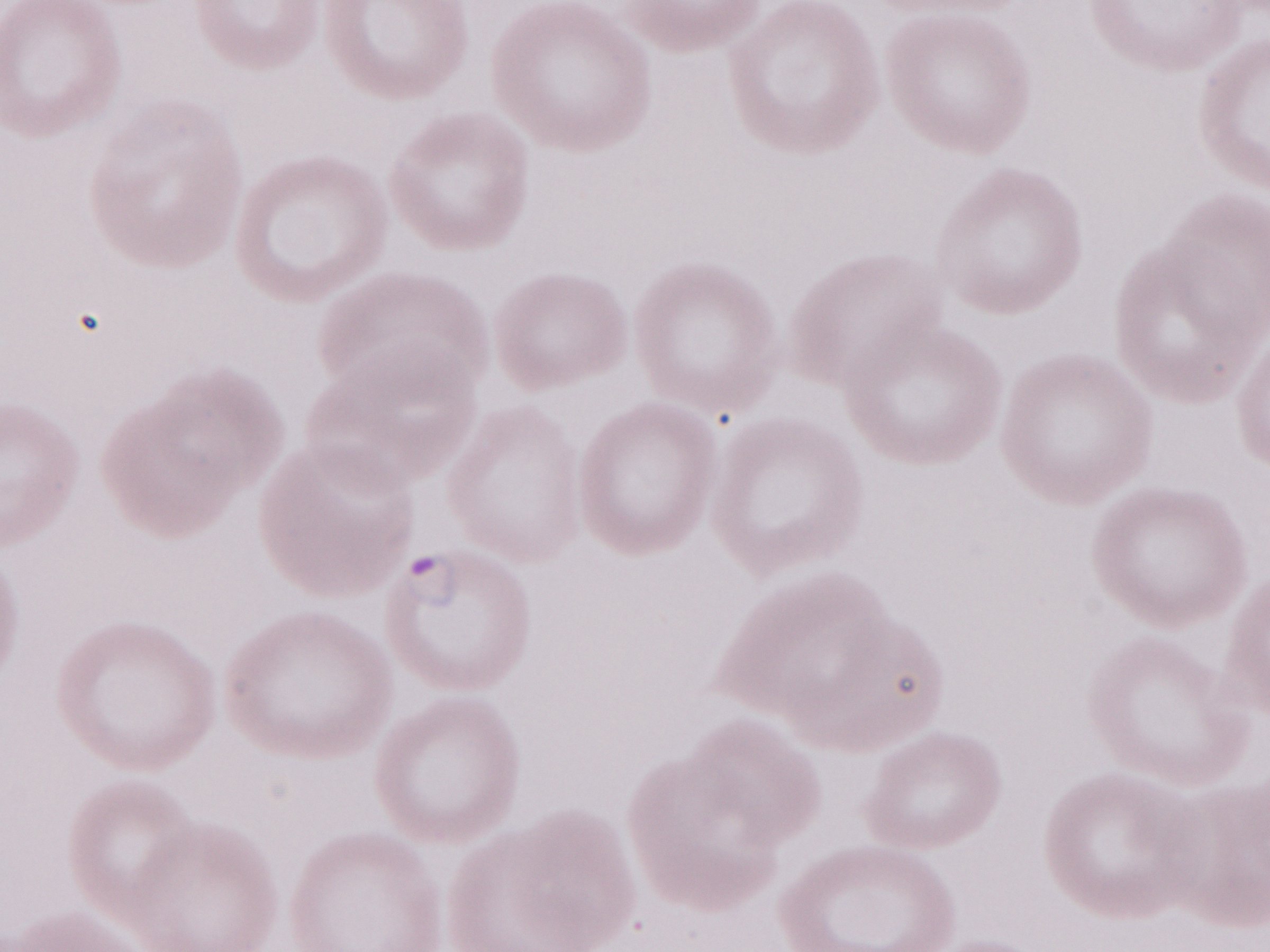
Thin blood smear. 1,000x magnification. May-Grünwald-Giemsa-stained preparation. Image is 1270×952 pixels. Patient diagnosis: malaria infection. One field of this slide. Olympus BX43 microscope and DP73 digital camera.